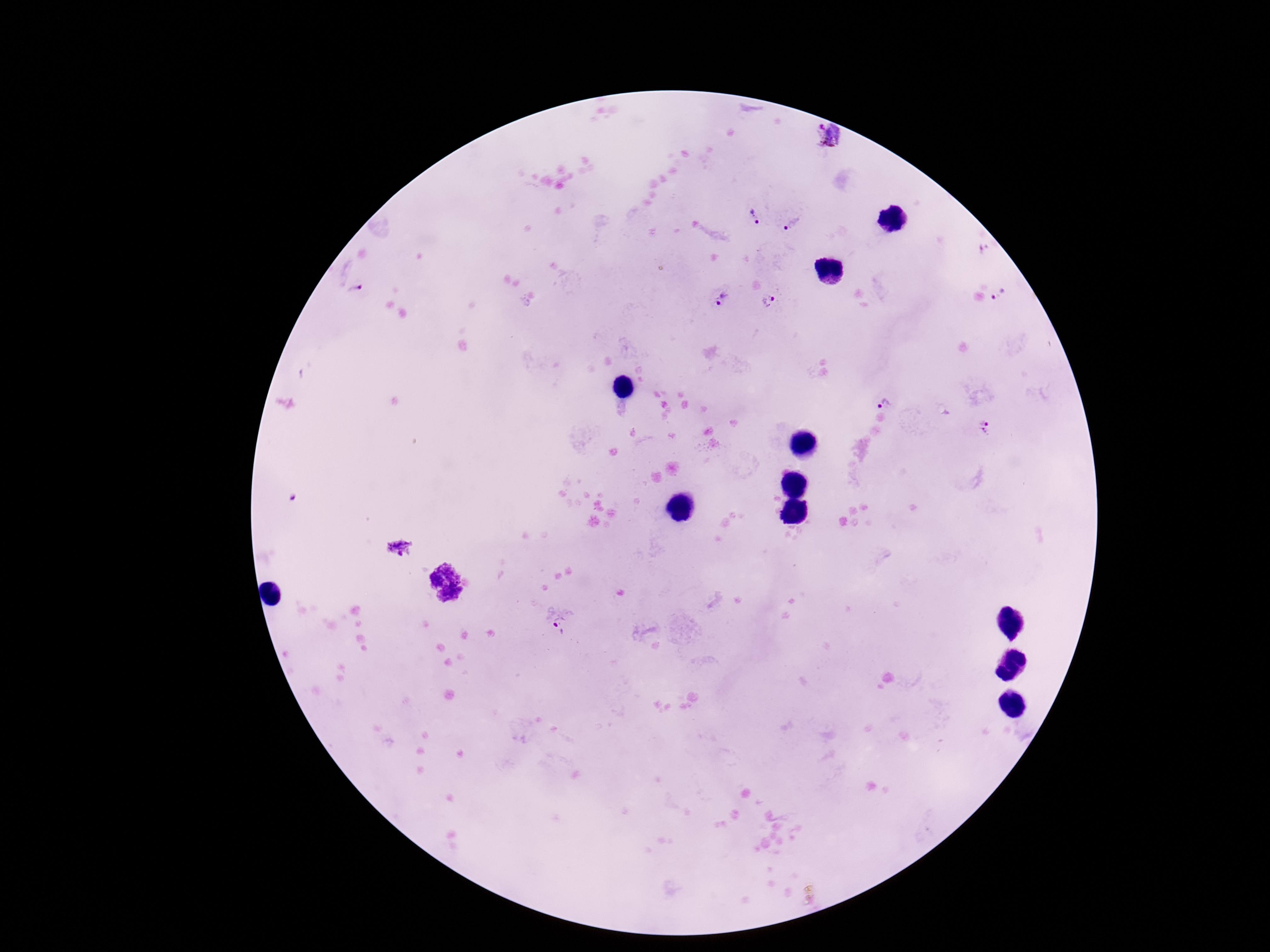
Approximate object centers, in pixels from the top-left corner.
Summary:
  - Plasmodium parasite locations: (x=827, y=136), (x=752, y=217), (x=791, y=225), (x=358, y=289), (x=998, y=298), (x=722, y=299), (x=769, y=301), (x=882, y=399), (x=985, y=428), (x=399, y=549), (x=561, y=628)
  - Preparation: thick blood smear
  - Stain: Giemsa
  - Image size: 1270×952 pixels
  - Patient malaria status: positive
  - Field of view: single
  - Capture: smartphone camera through the microscope eyepiece
  - Magnification: 100x